Classify this cell by malaria status.
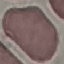
It is uninfected.

Acquired by smartphone through the microscope eyepiece. Thin blood smear. Giemsa stain. Cell patch, automatically extracted from a larger field of view and resized to 64 × 64 pixels.